Point out each Plasmodium parasite.
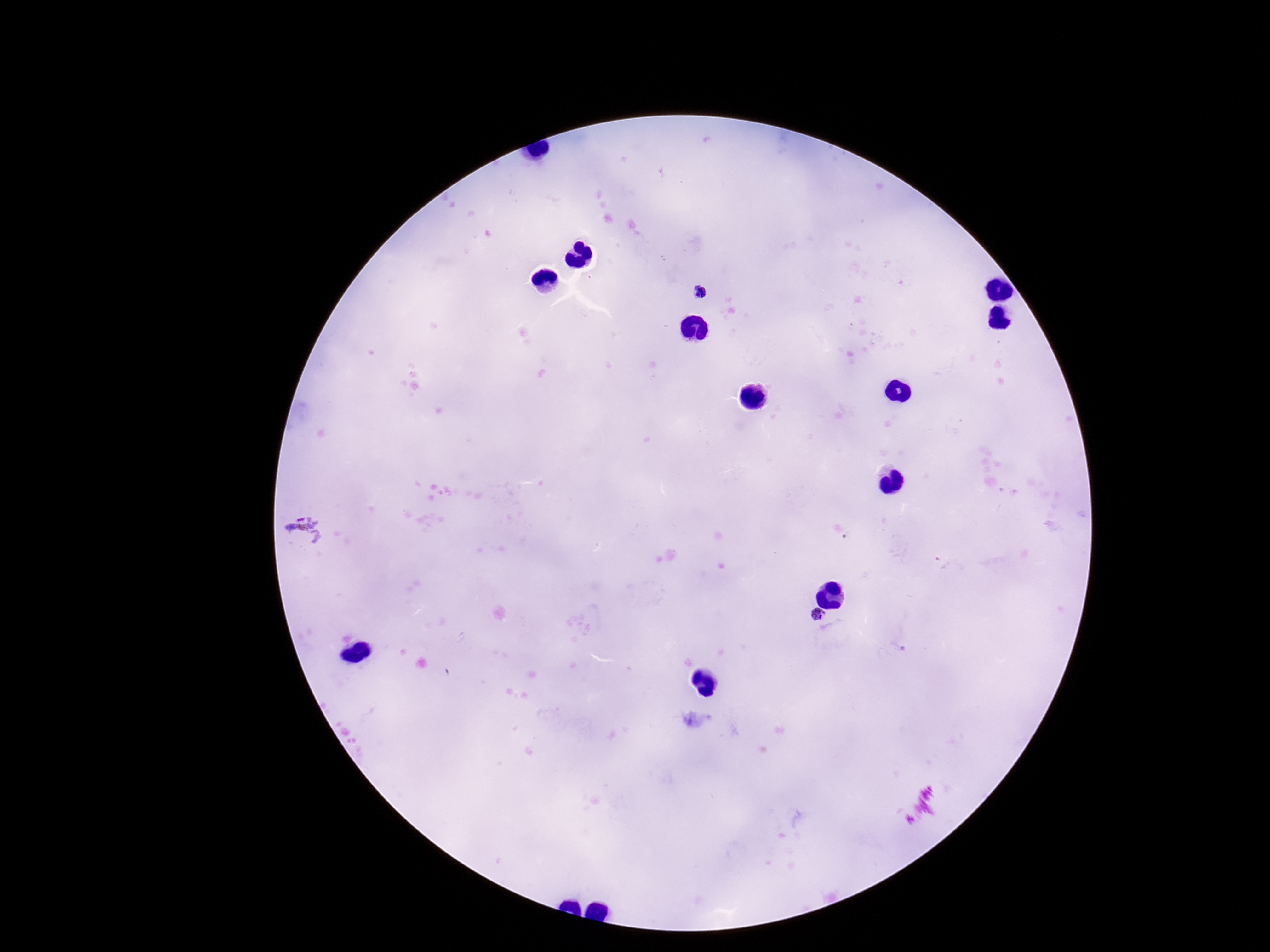

Approximate centers as (x, y) in pixels.
Plasmodium parasites: (702, 291), (819, 618).

Summary:
  - Image size: 1270×952 pixels
  - Patient malaria status: positive
  - Stain: Giemsa
  - Preparation: thick peripheral-blood smear
  - Magnification: 100x
  - Capture: smartphone camera through the microscope eyepiece
  - Field of view: single